State the preparation type.
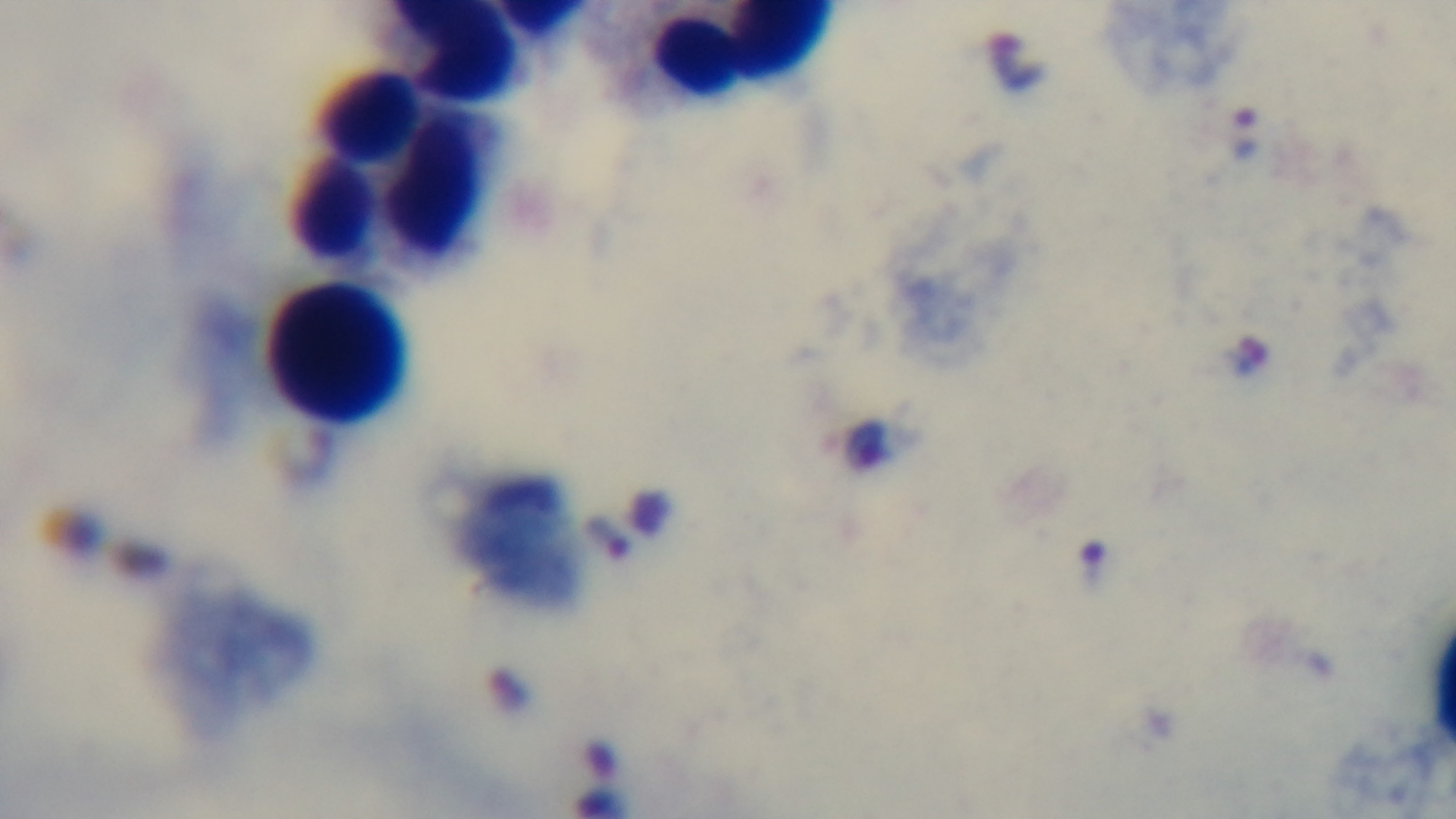

Thick.

objective = 100x oil immersion
malaria status = infected
modality = light microscopy
stain = Giemsa
field of view = single
capture = mounted 4K digital camera